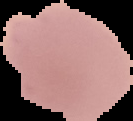
malaria status = uninfected
image type = cell region segmented out of the field of view; surrounding area masked to black
preparation = thin blood film
image size = 133×121 pixels